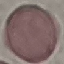
Summary:
  - Result: no malaria parasites seen
  - Stain: Giemsa
  - Image type: automatically extracted cell patch, resized to 64 × 64 pixels
  - Capture: smartphone through the microscope eyepiece
  - Preparation: thin smear